Comment on the morphology of the red blood cells.
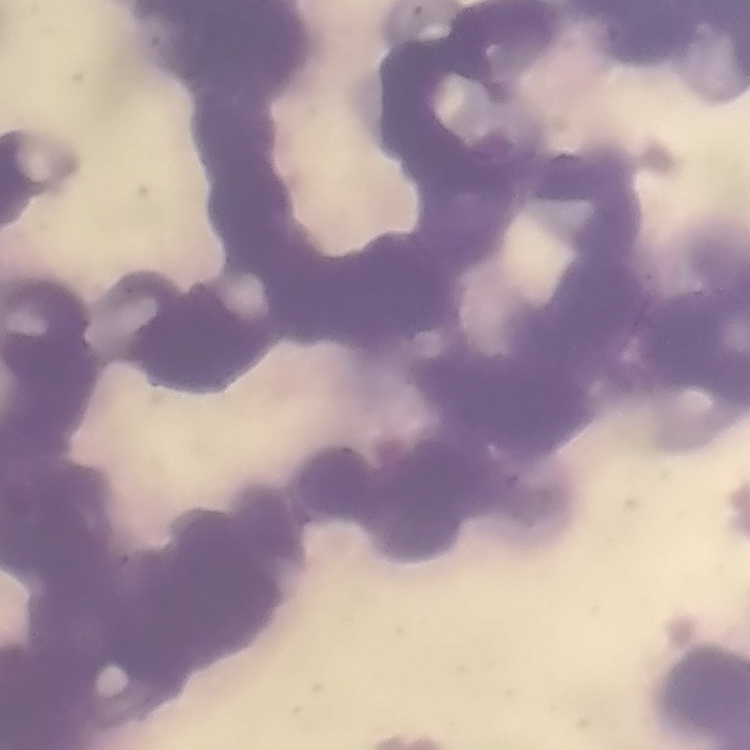

They show rouleaux formation.

preparation = thin peripheral smear
stain = Field's or Giemsa
image type = one tile cut from a larger photomicrograph